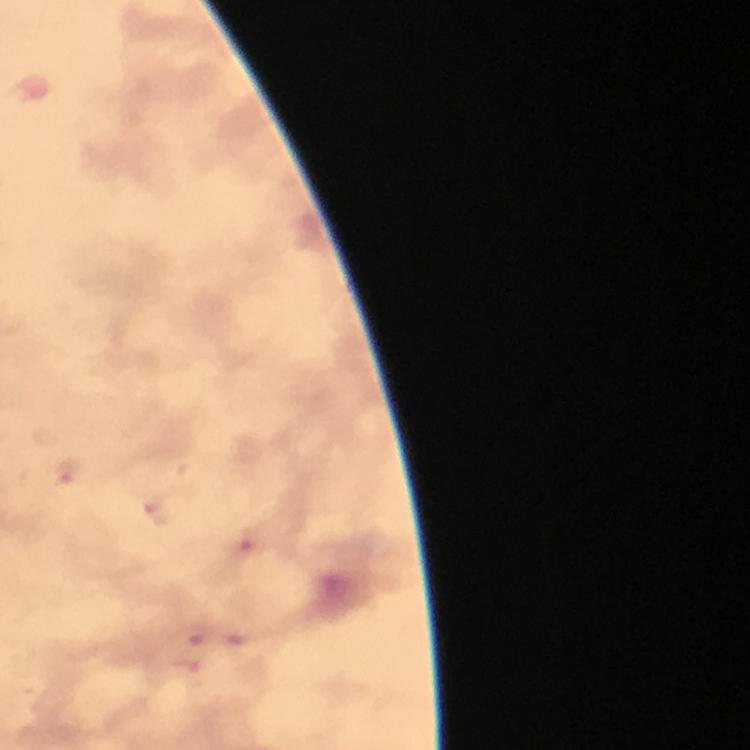

capture = smartphone photograph through a microscope
malaria parasite locations = approximate centers as [x, y] in pixels: [67, 473], [160, 513], [249, 549], [194, 634]
image size = 750×750 pixels
magnification = 100x
stain = Giemsa
preparation = thick blood smear
immersion oil = used
cropped from = a single field of view
context = from a malaria diagnostic workup